Locate every malaria parasite.
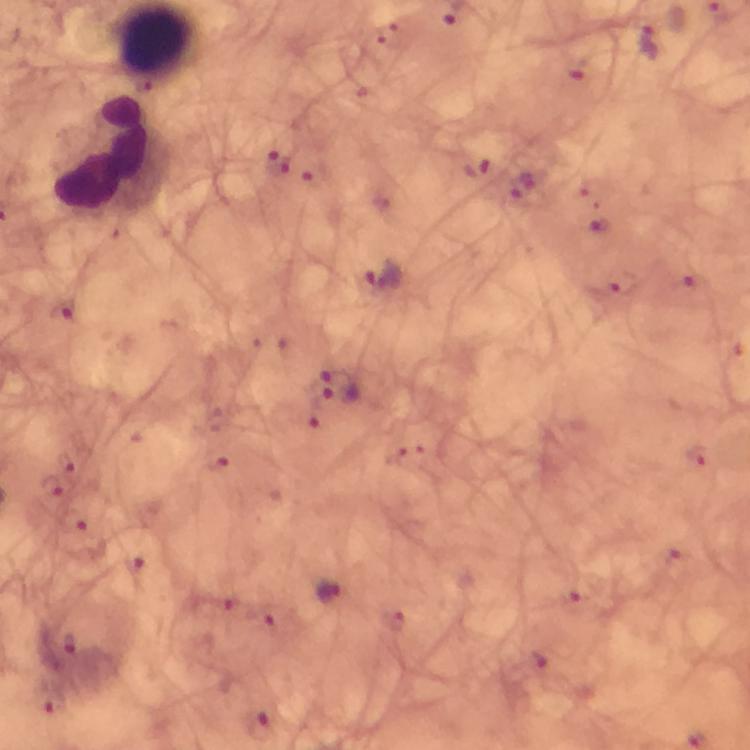

Approximate centers as {x, y} in pixels.
Malaria parasites: {648, 41}, {276, 164}, {385, 275}, {62, 309}, {333, 372}, {341, 393}, {328, 592}, {70, 644}.

Summary:
  - Leukocyte locations: {110, 155}
  - Image size: 750×750 pixels
  - Cropped from: a single field of view
  - Stain: Giemsa
  - Preparation: thick blood smear
  - Magnification: 100x
  - Capture: smartphone mounted on the microscope
  - Context: from a diagnostic examination for malaria
  - Immersion oil: applied